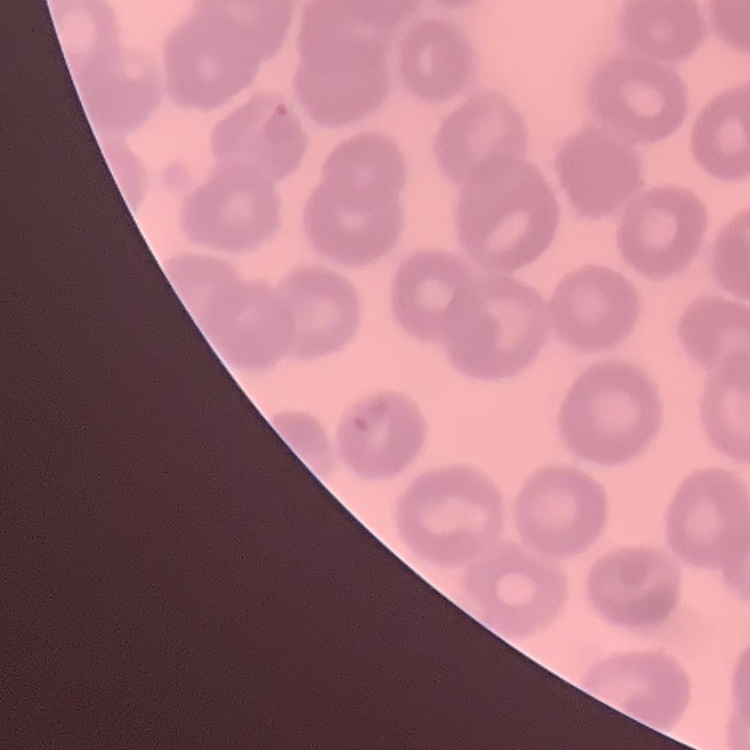 The erythrocytes show no rouleaux formation. Field's or Giemsa stain. One tile cut from a larger photomicrograph. Thin peripheral smear.